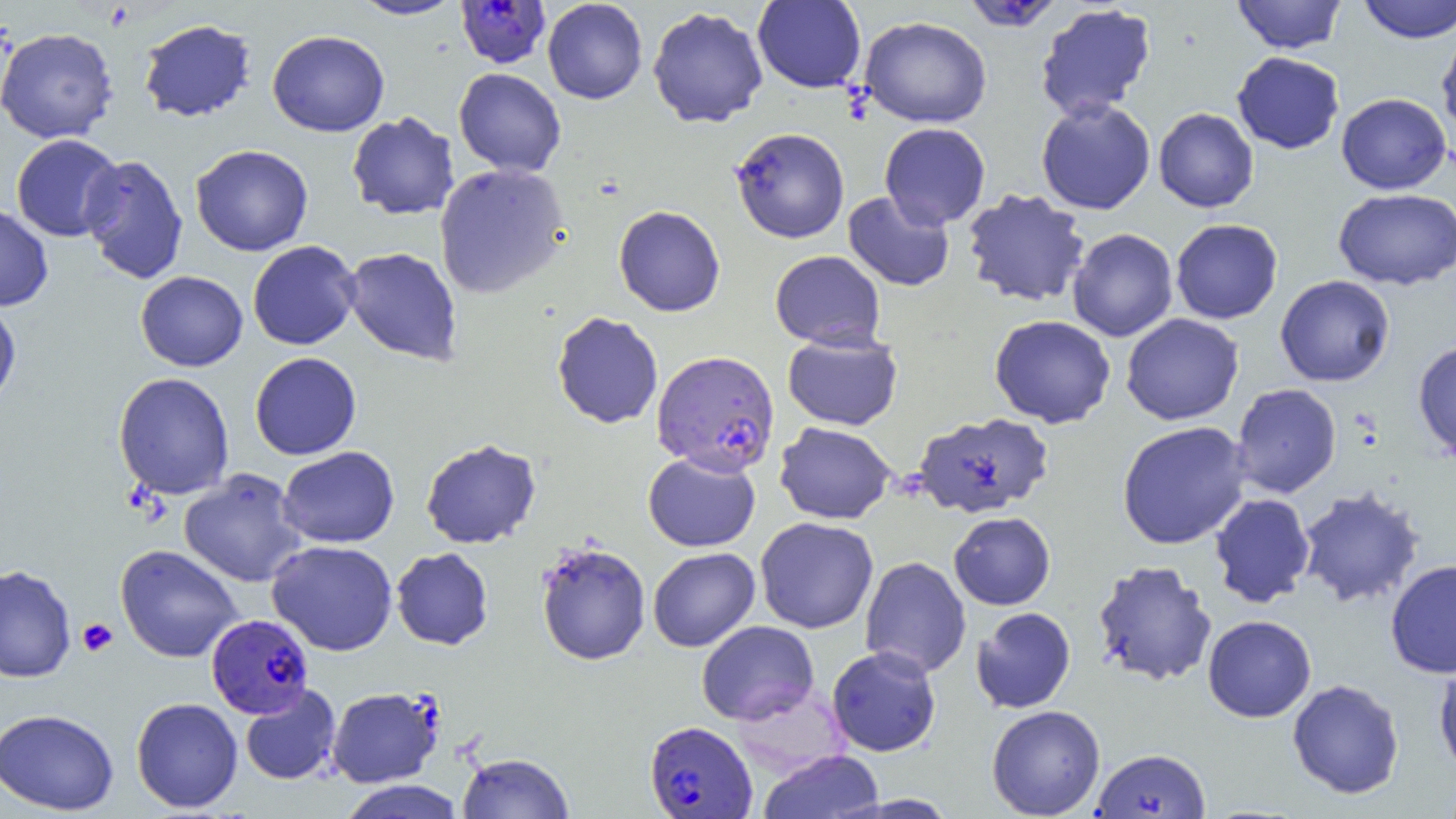
Summary:
  - Coordinate format: approximate bounding boxes as [x1, y1, x2, y2] in pixels
  - Plasmodium falciparum-infected red blood cell locations: [455, 0, 551, 69], [962, 0, 1062, 32], [652, 350, 781, 476], [206, 613, 314, 718], [644, 720, 757, 818]
  - Uninfected red blood cell locations: [348, 0, 464, 20], [542, 0, 648, 104], [753, 0, 866, 93], [1233, 0, 1346, 53], [1357, 0, 1456, 43], [1035, 3, 1157, 120], [647, 6, 768, 128], [859, 16, 992, 128], [138, 18, 256, 122], [0, 27, 118, 143], [1436, 27, 1456, 143], [267, 29, 390, 137], [1232, 51, 1345, 154], [453, 68, 566, 177], [1336, 92, 1452, 194], [1036, 98, 1156, 215], [1153, 107, 1259, 213], [346, 111, 460, 220], [879, 122, 991, 229], [730, 127, 850, 243], [11, 134, 123, 241], [190, 144, 313, 256], [79, 154, 188, 285], [433, 163, 570, 299], [1333, 187, 1456, 290], [961, 189, 1091, 308], [842, 191, 955, 292], [0, 204, 53, 311], [613, 205, 725, 317], [1170, 219, 1283, 324], [1067, 228, 1178, 342], [248, 240, 362, 350], [341, 247, 463, 367], [770, 250, 885, 349], [135, 270, 248, 372], [1275, 275, 1395, 387], [0, 301, 22, 411], [551, 311, 663, 429], [1121, 313, 1244, 425], [989, 315, 1116, 428], [782, 331, 903, 430], [1412, 340, 1456, 461], [249, 352, 362, 460], [113, 372, 235, 500], [1231, 383, 1341, 498], [912, 412, 1054, 519], [1116, 421, 1252, 550], [775, 422, 897, 525], [420, 438, 541, 549], [278, 446, 399, 548], [642, 452, 761, 552], [179, 469, 308, 588], [1296, 486, 1426, 609], [1210, 493, 1315, 608], [948, 511, 1056, 610], [755, 517, 878, 634], [267, 540, 398, 656], [535, 541, 651, 666], [115, 544, 243, 663], [391, 547, 493, 650], [648, 547, 760, 652], [859, 556, 971, 679], [1385, 559, 1456, 678], [1092, 560, 1218, 688], [0, 564, 76, 683], [971, 607, 1076, 714], [1202, 615, 1317, 722], [696, 620, 819, 726], [826, 645, 941, 756], [1433, 656, 1456, 779], [1287, 679, 1405, 799], [239, 683, 342, 786], [327, 686, 444, 788], [130, 697, 243, 813], [986, 704, 1105, 818], [0, 708, 119, 815], [1091, 748, 1210, 818], [758, 750, 885, 819], [457, 752, 574, 818], [337, 780, 466, 819]
  - Platelet locations: [77, 618, 118, 657]
  - Slide-level diagnosis: Plasmodium falciparum
  - Preparation: thin blood smear
  - Image size: 1456×819 pixels
  - Field of view: single
  - Magnification: 1000x
  - Modality: optical microscopy